Comment on the morphology of the red blood cells.
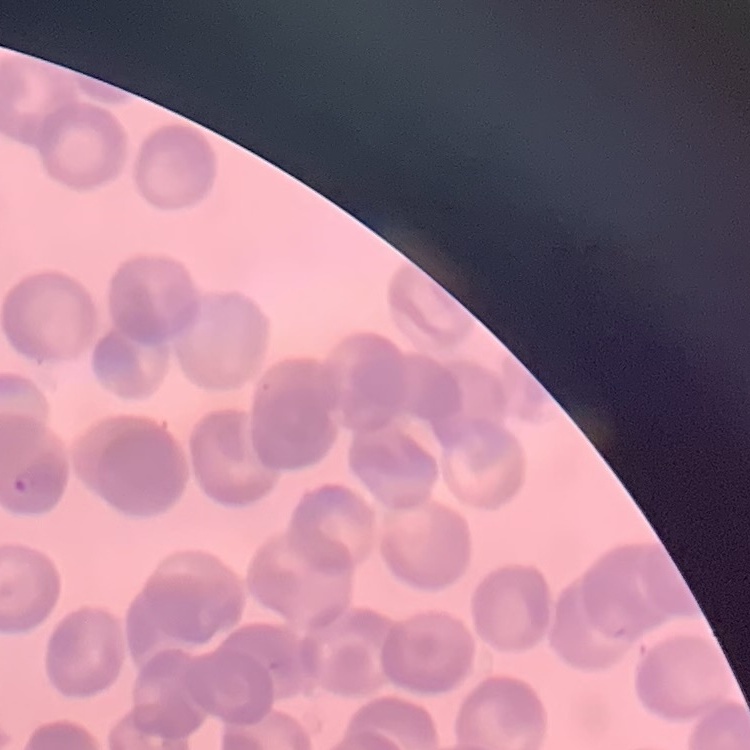

Rouleaux formation.

Field's or Giemsa stain. One tile cut from a larger photomicrograph. Thin blood film.